State which parasite is depicted.
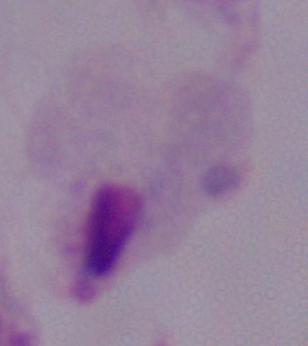
This is a trichomonad.

Summary:
  - Modality: photomicrograph
  - Magnification: 1000x